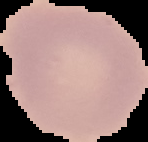

Summary:
  - Result: no Plasmodium parasites detected
  - Image type: segmented cell region on a black background
  - Image size: 148×142 pixels
  - Preparation: thin blood film